Name the blood parasite species.
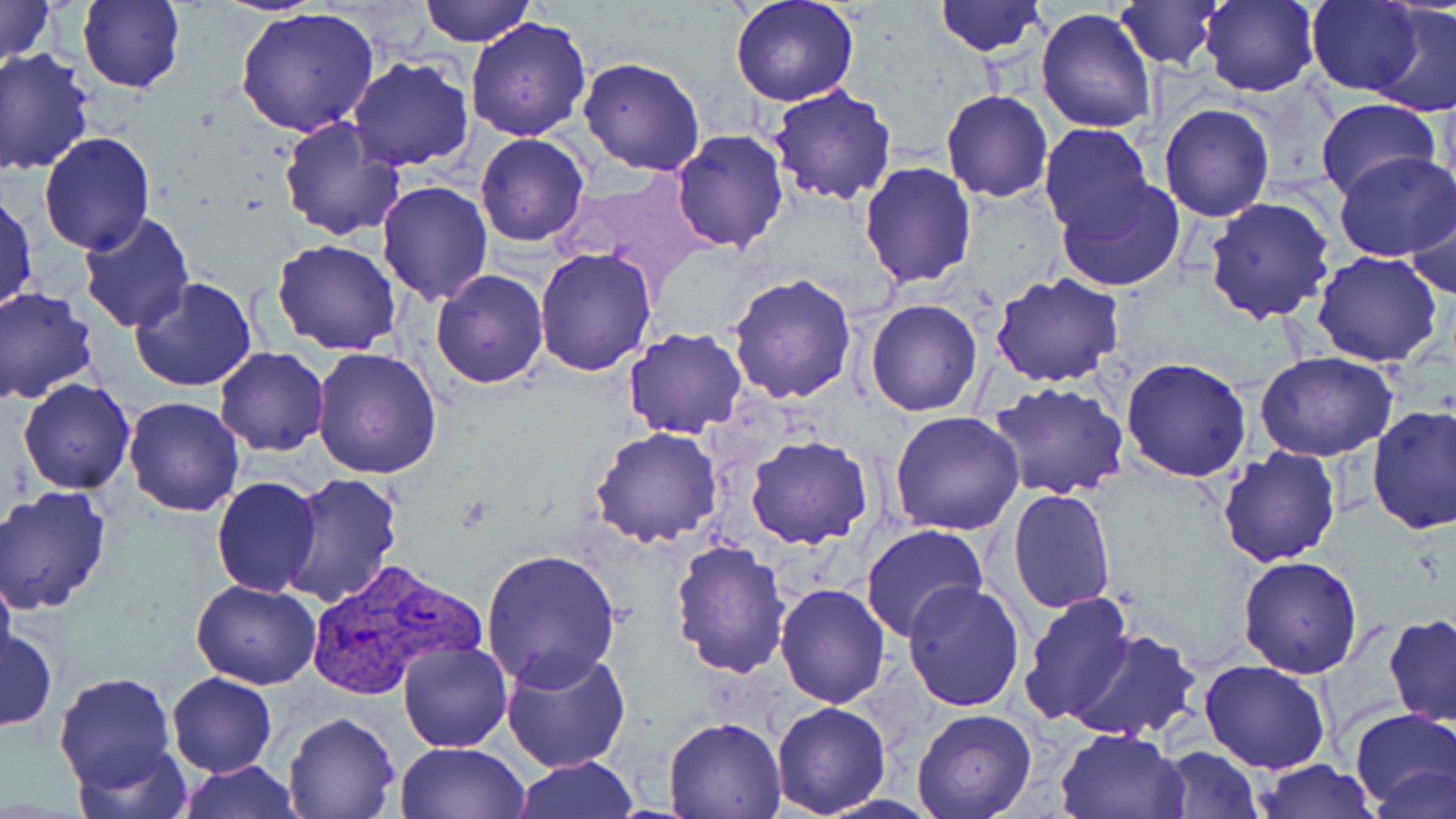

Plasmodium vivax.

{
  "magnification": "1000x",
  "uninfected_red_blood_cell_locations": "approximate bounding boxes as named x1/y1/x2/y2 corners in pixels: (x1=0, y1=0, x2=55, y2=73), (x1=78, y1=0, x2=184, y2=93), (x1=418, y1=0, x2=533, y2=47), (x1=729, y1=0, x2=860, y2=107), (x1=934, y1=0, x2=1046, y2=57), (x1=1110, y1=1, x2=1227, y2=71), (x1=1198, y1=1, x2=1322, y2=97), (x1=1307, y1=1, x2=1426, y2=95), (x1=1369, y1=4, x2=1455, y2=118), (x1=237, y1=7, x2=379, y2=139), (x1=1037, y1=7, x2=1158, y2=135), (x1=464, y1=15, x2=593, y2=140), (x1=0, y1=49, x2=96, y2=176), (x1=346, y1=56, x2=474, y2=171), (x1=579, y1=56, x2=705, y2=176), (x1=767, y1=84, x2=897, y2=206), (x1=941, y1=90, x2=1053, y2=203), (x1=1313, y1=97, x2=1441, y2=202), (x1=1159, y1=103, x2=1274, y2=220), (x1=277, y1=115, x2=406, y2=242), (x1=1040, y1=123, x2=1156, y2=239), (x1=671, y1=129, x2=789, y2=253), (x1=39, y1=133, x2=155, y2=255), (x1=474, y1=133, x2=590, y2=248), (x1=1333, y1=150, x2=1456, y2=260), (x1=859, y1=161, x2=977, y2=288), (x1=1055, y1=178, x2=1186, y2=294), (x1=375, y1=180, x2=493, y2=303), (x1=1, y1=188, x2=37, y2=317), (x1=1406, y1=190, x2=1455, y2=301), (x1=1203, y1=195, x2=1335, y2=324), (x1=78, y1=212, x2=197, y2=333), (x1=271, y1=238, x2=401, y2=355), (x1=534, y1=246, x2=658, y2=378), (x1=1311, y1=251, x2=1444, y2=367), (x1=430, y1=269, x2=549, y2=388), (x1=992, y1=273, x2=1126, y2=389), (x1=728, y1=274, x2=857, y2=405), (x1=129, y1=276, x2=257, y2=391), (x1=0, y1=287, x2=99, y2=405), (x1=865, y1=299, x2=983, y2=416), (x1=622, y1=327, x2=748, y2=438), (x1=214, y1=346, x2=330, y2=456), (x1=312, y1=348, x2=442, y2=480), (x1=1255, y1=351, x2=1398, y2=461), (x1=1122, y1=355, x2=1253, y2=481), (x1=18, y1=377, x2=136, y2=494), (x1=987, y1=379, x2=1129, y2=499), (x1=123, y1=395, x2=245, y2=515), (x1=1367, y1=405, x2=1456, y2=534), (x1=889, y1=411, x2=1024, y2=536), (x1=590, y1=426, x2=724, y2=547), (x1=745, y1=434, x2=873, y2=549), (x1=1217, y1=447, x2=1341, y2=567), (x1=283, y1=474, x2=402, y2=608), (x1=211, y1=476, x2=322, y2=596), (x1=1, y1=488, x2=113, y2=614), (x1=1008, y1=488, x2=1116, y2=612), (x1=860, y1=525, x2=986, y2=643), (x1=672, y1=539, x2=792, y2=679), (x1=478, y1=548, x2=624, y2=689), (x1=1238, y1=556, x2=1363, y2=677), (x1=0, y1=565, x2=16, y2=678), (x1=191, y1=578, x2=323, y2=688), (x1=775, y1=581, x2=890, y2=707), (x1=903, y1=581, x2=1025, y2=712), (x1=1018, y1=590, x2=1136, y2=727), (x1=1382, y1=615, x2=1456, y2=727), (x1=1, y1=627, x2=58, y2=732), (x1=1064, y1=628, x2=1200, y2=742), (x1=397, y1=641, x2=514, y2=752), (x1=500, y1=646, x2=632, y2=773), (x1=1199, y1=658, x2=1331, y2=773), (x1=54, y1=671, x2=177, y2=795), (x1=166, y1=673, x2=276, y2=777), (x1=771, y1=702, x2=892, y2=817), (x1=1350, y1=707, x2=1456, y2=810), (x1=911, y1=708, x2=1038, y2=819), (x1=283, y1=712, x2=399, y2=819), (x1=661, y1=716, x2=785, y2=818), (x1=1055, y1=726, x2=1187, y2=818), (x1=73, y1=740, x2=192, y2=819), (x1=396, y1=742, x2=529, y2=819), (x1=1158, y1=745, x2=1262, y2=817), (x1=511, y1=756, x2=642, y2=817), (x1=1254, y1=759, x2=1378, y2=817), (x1=177, y1=760, x2=300, y2=819), (x1=1369, y1=762, x2=1454, y2=819)",
  "field_of_view": "single",
  "modality": "light microscopy",
  "plasmodium_vivax_infected_red_blood_cell_locations": "approximate bounding boxes as named x1/y1/x2/y2 corners in pixels: (x1=300, y1=558, x2=486, y2=704)",
  "preparation": "thin blood smear",
  "stain": "May-Grünwald-Giemsa",
  "image_size": "1456×819 pixels"
}